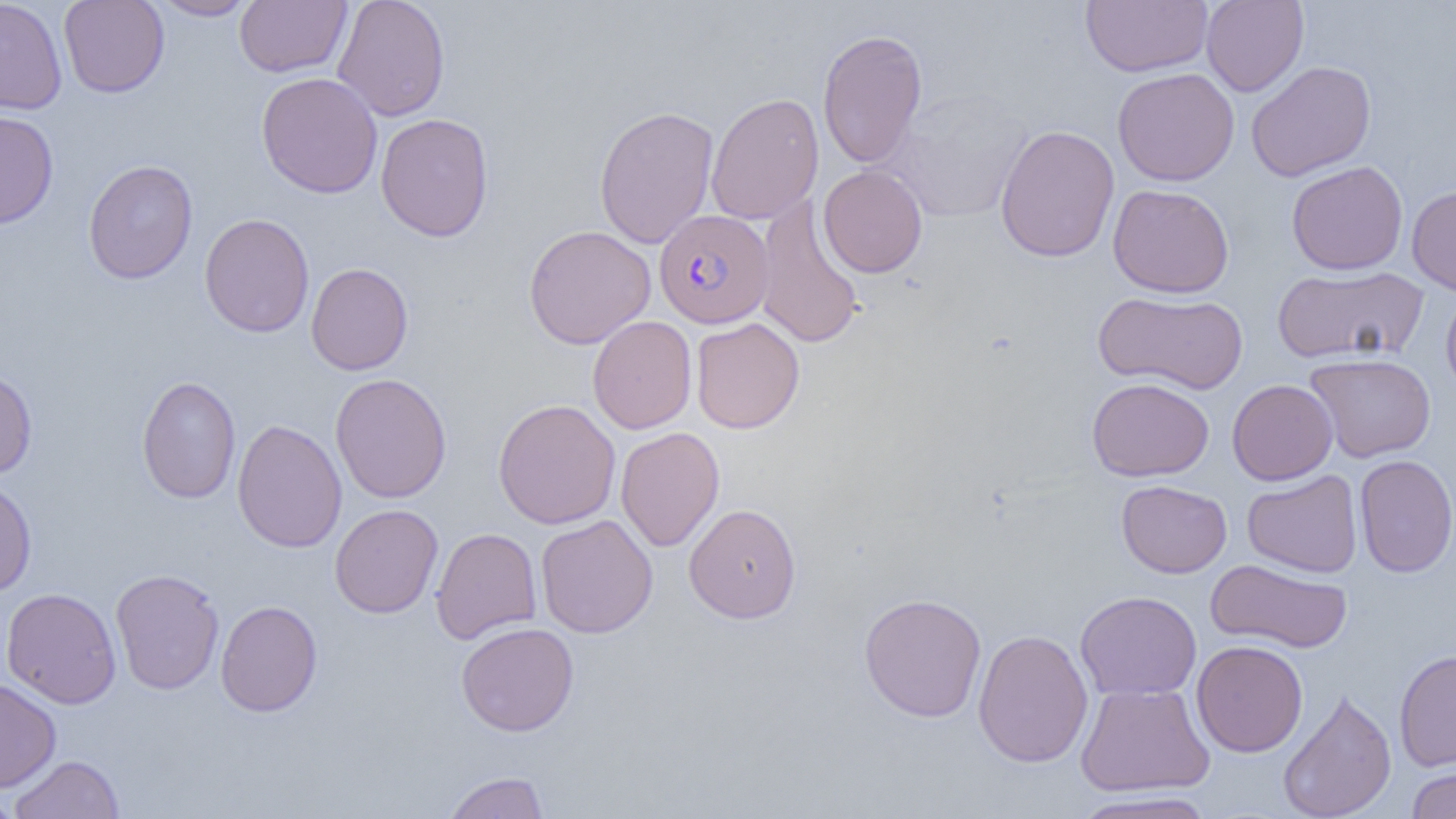

slide-level diagnosis = Plasmodium falciparum
preparation = thin blood film
modality = optical microscopy
magnification = 1000x
field of view = single
image size = 1456×819 pixels
uninfected red blood cell locations = approximate bounding boxes as (x1,y1)-(x2,y2) corner pairs in pixels: (0,0)-(68,115), (58,0)-(170,98), (150,0)-(259,21), (234,0)-(352,77), (332,0)-(450,122), (1080,0)-(1212,77), (1201,0)-(1309,97), (817,29)-(928,168), (1246,60)-(1377,181), (1112,67)-(1240,186), (256,72)-(383,199), (883,90)-(1034,224), (705,92)-(824,225), (593,105)-(719,249), (0,111)-(59,229), (375,113)-(494,242), (994,124)-(1120,262), (83,159)-(198,284), (1286,160)-(1408,275), (818,165)-(928,278), (1107,183)-(1235,298), (1406,185)-(1456,296), (753,197)-(865,350), (199,213)-(314,337), (523,224)-(656,349), (306,262)-(413,375), (1272,265)-(1428,365), (1441,287)-(1456,400), (1093,290)-(1248,395), (587,315)-(697,434), (690,317)-(805,434), (1304,353)-(1436,462), (0,368)-(37,479), (330,373)-(451,503), (136,376)-(241,503), (1086,377)-(1214,481), (1227,379)-(1338,485), (493,399)-(621,529), (232,419)-(347,553), (615,427)-(724,552), (1354,454)-(1456,578), (1242,470)-(1363,578), (0,478)-(37,597), (1116,480)-(1232,578), (330,503)-(443,618), (684,503)-(801,623), (535,514)-(658,638), (431,527)-(542,644), (1205,558)-(1353,654), (110,568)-(225,695), (1,587)-(122,708), (1075,590)-(1202,700), (858,592)-(987,723), (215,599)-(322,717), (456,622)-(579,736), (972,629)-(1093,768), (1191,640)-(1308,757), (1394,648)-(1456,771), (0,678)-(61,792), (1075,682)-(1214,796), (1278,687)-(1396,819), (10,754)-(124,819), (1405,765)-(1456,819), (442,772)-(550,819), (1068,790)-(1220,819), (0,791)-(23,818)
Plasmodium falciparum-infected red blood cell locations = approximate bounding boxes as (x1,y1)-(x2,y2) corner pairs in pixels: (654,208)-(773,328)